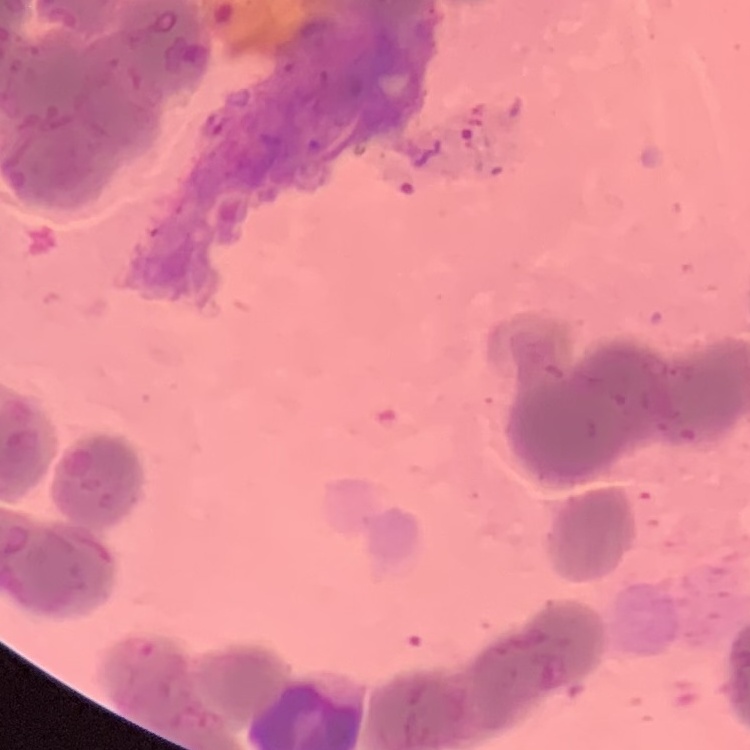

Summary:
  - Erythrocyte morphology: rouleaux formation
  - Stain: Field's or Giemsa
  - Image type: one tile cut from a larger photomicrograph
  - Preparation: thin blood film